Point out each Plasmodium parasite.
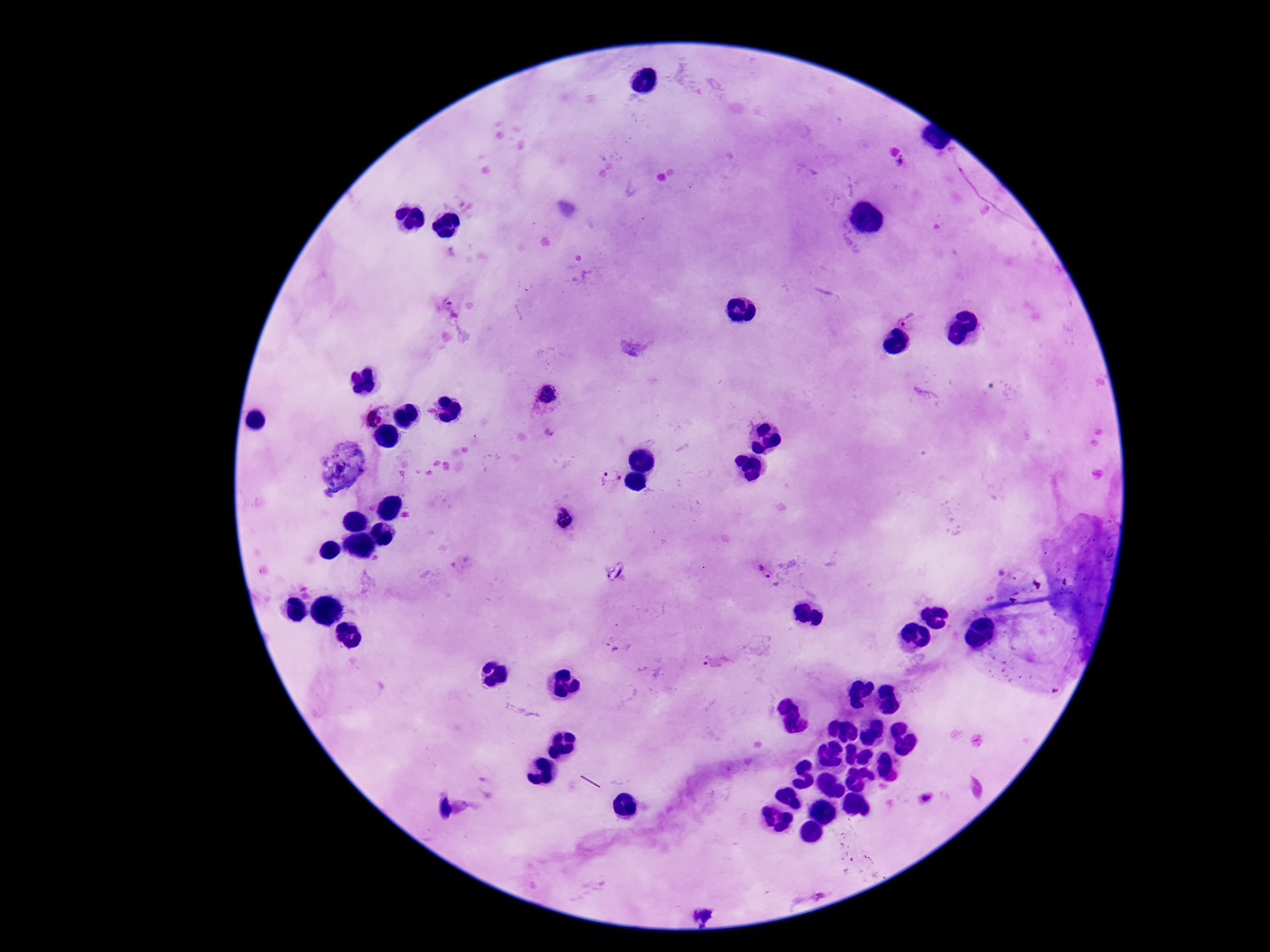

Approximate centers as (x, y) in pixels.
Plasmodium parasites: (902, 163), (451, 307), (909, 320), (548, 398), (372, 417), (548, 433), (610, 477), (764, 571), (705, 660).

Thick blood film. 100x magnification. Photographed through the microscope eyepiece with a smartphone camera. Giemsa stain. Image is 1270×952 pixels. Patient malaria status: infected. One field from this slide.